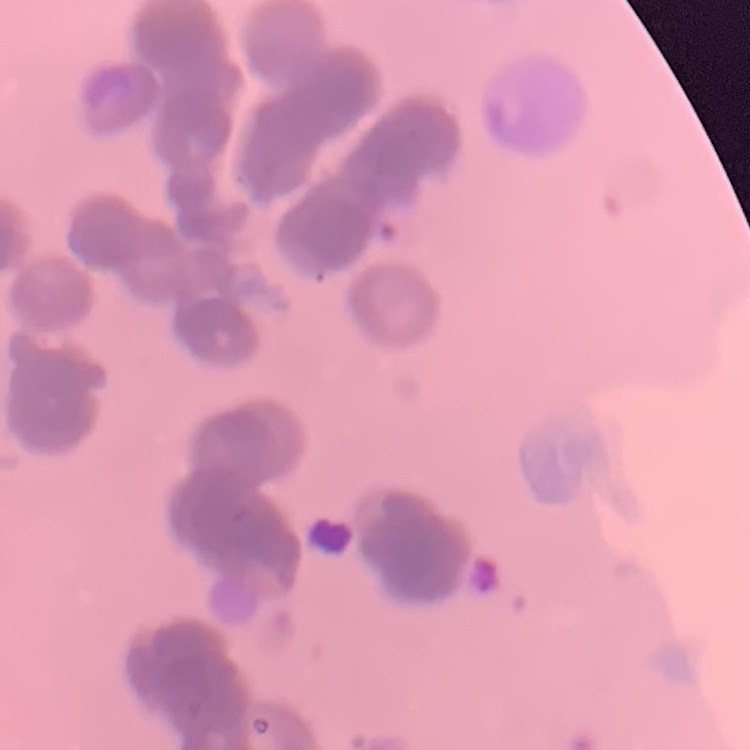 The red blood cells show rouleaux formation. Field's or Giemsa stain. Square crop of a larger photomicrograph. Thin blood film.